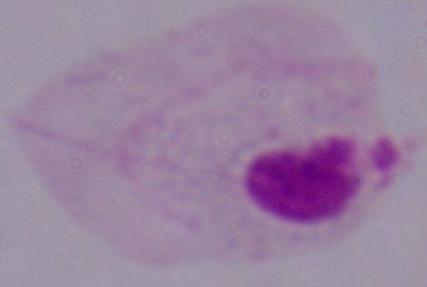

modality = photomicrograph
magnification = 1000x
identification = trichomonad